Locate every blood parasite and identify its species.
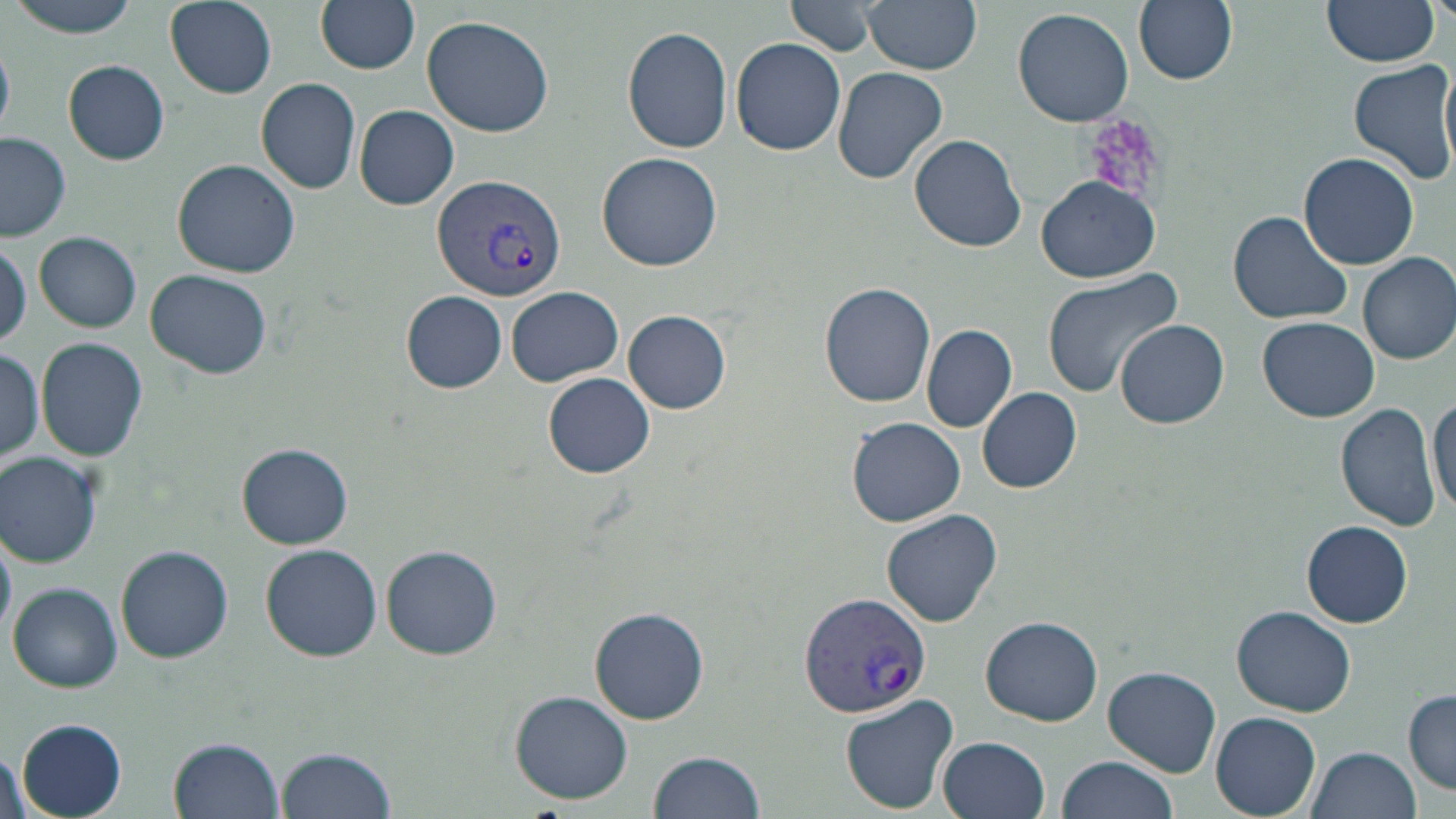
Approximate bounding boxes as (x1, y1, x2, y2) in pixels.
Plasmodium vivax-infected red blood cells: (430, 172, 568, 303), (798, 588, 933, 718).
No Plasmodium falciparum, Plasmodium ovale, Plasmodium malariae, Babesia divergens, or Trypanosoma brucei observed.

Platelet locations: (1082, 112, 1172, 199). Uninfected red blood cell locations: (7, 0, 145, 38), (315, 0, 420, 74), (787, 0, 882, 57), (862, 0, 984, 72), (1134, 0, 1238, 86), (1322, 0, 1439, 68), (166, 1, 278, 98), (1013, 7, 1135, 128), (421, 15, 554, 136), (623, 26, 733, 154), (732, 37, 846, 155), (63, 59, 170, 164), (1349, 60, 1456, 187), (831, 65, 950, 185), (256, 77, 361, 193), (353, 105, 459, 210), (0, 132, 73, 242), (910, 135, 1027, 252), (597, 152, 724, 272), (1299, 152, 1419, 271), (172, 159, 302, 278), (1036, 175, 1162, 283), (1228, 209, 1354, 325), (34, 231, 142, 332), (0, 235, 30, 350), (1357, 252, 1456, 364), (1041, 268, 1184, 396), (147, 270, 272, 381), (820, 282, 936, 407), (507, 288, 624, 386), (402, 291, 506, 393), (624, 310, 731, 413), (1257, 316, 1380, 423), (1116, 319, 1229, 429), (921, 324, 1017, 433), (39, 338, 149, 463), (0, 346, 45, 466), (543, 371, 655, 478), (977, 386, 1083, 493), (1429, 394, 1456, 517), (1336, 403, 1443, 532), (847, 417, 965, 527), (862, 422, 983, 619), (237, 442, 353, 549), (1, 452, 102, 567), (881, 508, 1003, 627), (1302, 520, 1413, 628), (0, 523, 16, 646), (260, 544, 383, 661), (381, 544, 502, 660), (117, 546, 232, 661), (9, 582, 122, 691), (1232, 605, 1356, 717), (589, 606, 710, 725), (981, 615, 1103, 726), (1104, 666, 1221, 777), (1404, 689, 1456, 793), (510, 690, 632, 804), (840, 695, 959, 812), (1211, 712, 1321, 816), (15, 719, 128, 816), (937, 735, 1050, 819), (168, 736, 283, 819), (276, 746, 397, 819), (1308, 746, 1422, 819), (0, 748, 31, 819), (649, 750, 764, 819), (1055, 756, 1177, 819). Slide-level diagnosis: Plasmodium vivax. 1000x magnification. May-Grünwald-Giemsa stain. Thin blood smear. Image is 1456×819 pixels. Optical microscopy. Single field of view.